Outline each blood parasite and name the species.
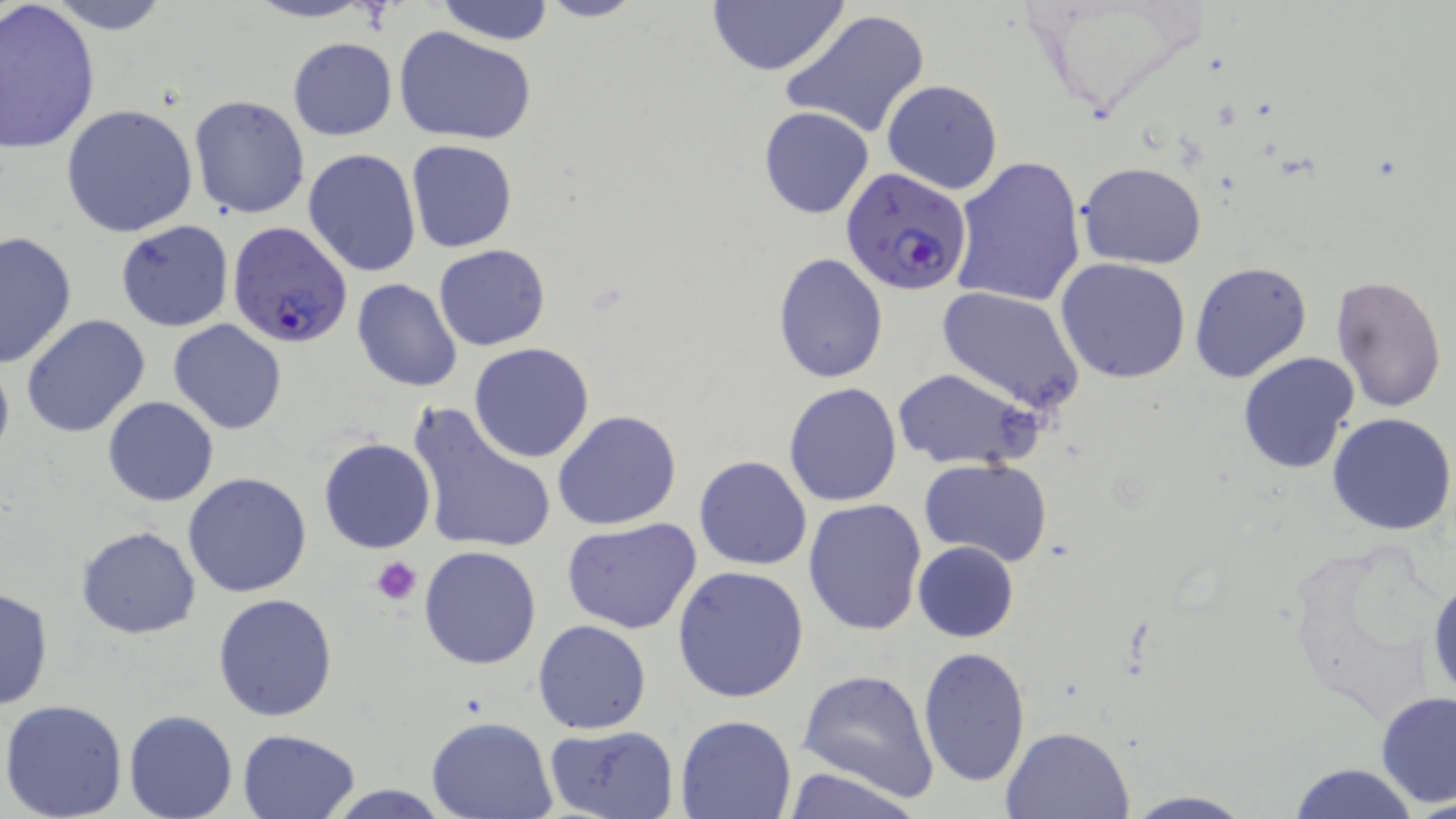
Approximate bounding boxes as named x1/y1/x2/y2 corners in pixels.
Plasmodium falciparum-infected red blood cells: (x1=840, y1=168, x2=973, y2=297), (x1=227, y1=221, x2=353, y2=348).
No Plasmodium ovale, Plasmodium malariae, Plasmodium vivax, Babesia divergens, or Trypanosoma brucei observed.

slide-level diagnosis = Plasmodium falciparum
image size = 1456×819 pixels
stain = May-Grünwald-Giemsa
modality = light microscopy
preparation = thin blood film
field of view = one of a larger specimen
platelet locations = approximate bounding boxes as named x1/y1/x2/y2 corners in pixels: (x1=371, y1=557, x2=421, y2=605)
uninfected red blood cell locations = approximate bounding boxes as named x1/y1/x2/y2 corners in pixels: (x1=41, y1=0, x2=178, y2=33), (x1=240, y1=0, x2=383, y2=23), (x1=433, y1=0, x2=556, y2=44), (x1=535, y1=0, x2=645, y2=23), (x1=705, y1=1, x2=849, y2=77), (x1=0, y1=2, x2=102, y2=156), (x1=779, y1=9, x2=931, y2=141), (x1=394, y1=25, x2=537, y2=144), (x1=287, y1=38, x2=396, y2=141), (x1=882, y1=80, x2=1003, y2=194), (x1=188, y1=95, x2=311, y2=220), (x1=61, y1=104, x2=198, y2=237), (x1=756, y1=105, x2=875, y2=218), (x1=405, y1=139, x2=517, y2=253), (x1=302, y1=147, x2=421, y2=277), (x1=951, y1=157, x2=1085, y2=307), (x1=1078, y1=162, x2=1205, y2=269), (x1=116, y1=219, x2=234, y2=332), (x1=0, y1=228, x2=77, y2=369), (x1=433, y1=244, x2=551, y2=351), (x1=773, y1=252, x2=889, y2=382), (x1=1055, y1=258, x2=1192, y2=384), (x1=1189, y1=262, x2=1313, y2=383), (x1=1331, y1=274, x2=1448, y2=413), (x1=352, y1=278, x2=463, y2=392), (x1=937, y1=286, x2=1084, y2=414), (x1=21, y1=314, x2=151, y2=439), (x1=168, y1=320, x2=288, y2=435), (x1=469, y1=342, x2=596, y2=463), (x1=1237, y1=351, x2=1360, y2=474), (x1=0, y1=352, x2=14, y2=466), (x1=890, y1=368, x2=1046, y2=473), (x1=784, y1=382, x2=903, y2=506), (x1=103, y1=396, x2=218, y2=506), (x1=407, y1=403, x2=557, y2=557), (x1=552, y1=409, x2=682, y2=531), (x1=1328, y1=412, x2=1455, y2=535), (x1=318, y1=438, x2=435, y2=553), (x1=694, y1=454, x2=813, y2=571), (x1=919, y1=458, x2=1055, y2=568), (x1=183, y1=471, x2=313, y2=596), (x1=803, y1=498, x2=926, y2=635), (x1=561, y1=518, x2=703, y2=635), (x1=75, y1=526, x2=201, y2=640), (x1=913, y1=540, x2=1018, y2=641), (x1=419, y1=545, x2=542, y2=668), (x1=671, y1=565, x2=809, y2=704), (x1=1427, y1=570, x2=1456, y2=701), (x1=0, y1=586, x2=54, y2=710), (x1=213, y1=593, x2=340, y2=722), (x1=532, y1=620, x2=652, y2=734), (x1=918, y1=645, x2=1031, y2=786), (x1=797, y1=669, x2=939, y2=799), (x1=1376, y1=690, x2=1456, y2=807), (x1=0, y1=699, x2=129, y2=819), (x1=123, y1=710, x2=237, y2=819), (x1=675, y1=713, x2=797, y2=817), (x1=427, y1=716, x2=557, y2=818), (x1=543, y1=724, x2=678, y2=817), (x1=1000, y1=725, x2=1135, y2=817), (x1=237, y1=728, x2=362, y2=819), (x1=1286, y1=762, x2=1420, y2=819), (x1=781, y1=763, x2=925, y2=819), (x1=320, y1=783, x2=456, y2=818), (x1=1122, y1=791, x2=1257, y2=818)
magnification = 1000x